Locate every Plasmodium parasite.
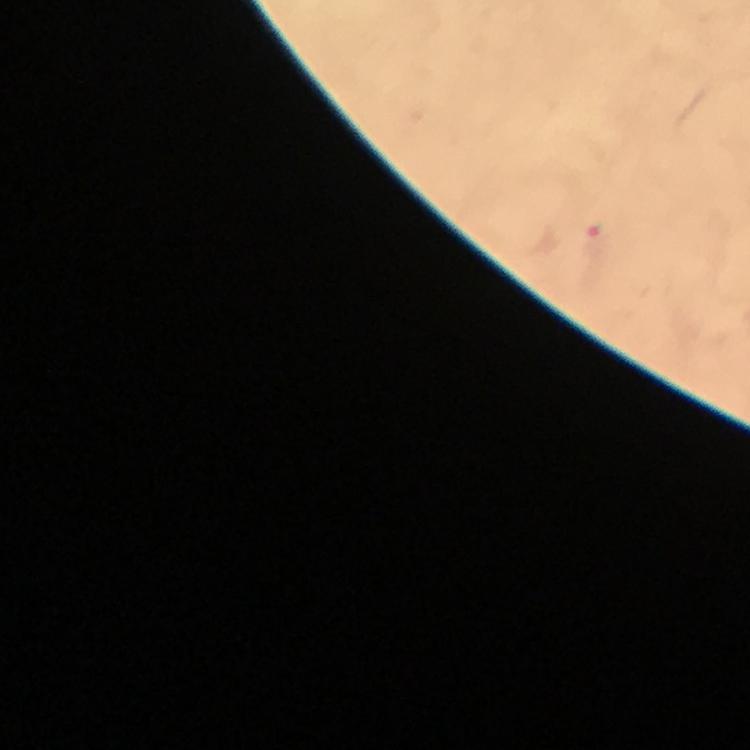

Approximate centers as {x, y} in pixels.
Plasmodium parasites: {593, 243}.

Immersion oil was used. Giemsa-stained preparation. At 100x magnification. Image is 750×750 pixels. From a malaria diagnostic workup. A crop from one field of view. Smartphone photograph taken through a microscope. Thick smear.